Give the position of every malaria parasite and every leukocyte.
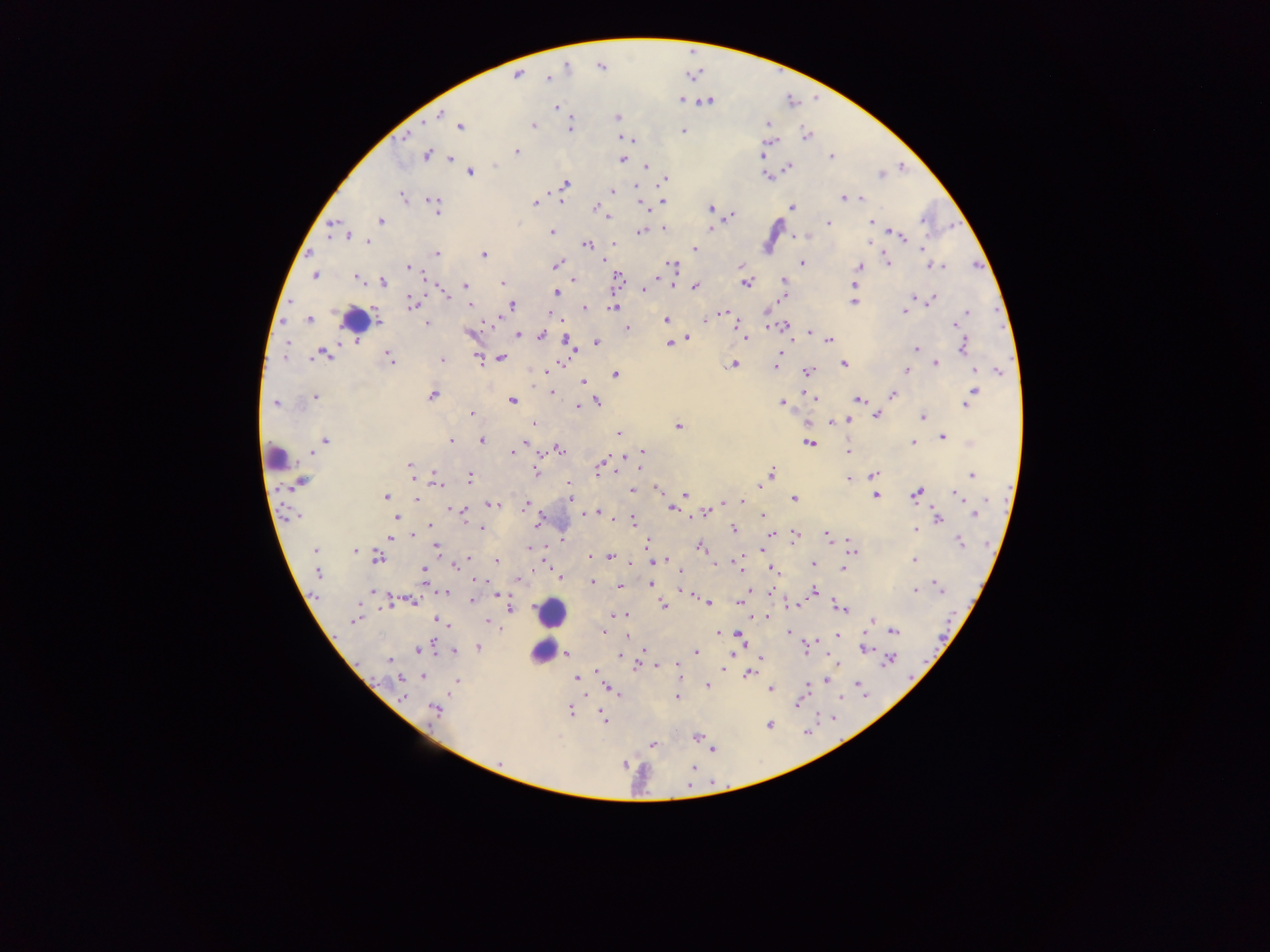
Approximate centers as x y in pixels.
Malaria parasites: 567 69; 517 75; 547 78; 680 100; 708 101; 558 107; 617 116; 436 117; 534 124; 766 125; 459 126; 570 129; 685 131; 806 134; 404 139; 769 140; 516 151; 426 154; 765 155; 831 155; 623 158; 646 165; 789 168; 471 171; 880 174; 770 176; 665 179; 566 182; 635 188; 612 192; 400 196; 862 198; 844 199; 430 200; 534 201; 560 202; 663 202; 437 205; 595 207; 791 207; 645 208; 708 209; 732 215; 605 217; 379 219; 829 222; 870 222; 331 226; 711 227; 662 229; 550 231; 639 231; 898 235; 367 243; 868 243; 588 244; 693 247; 922 248; 437 253; 483 255; 308 256; 601 258; 889 262; 556 263; 802 263; 673 265; 860 266; 406 267; 938 267; 313 276; 354 277; 619 279; 384 281; 425 281; 501 281; 573 282; 747 283; 463 285; 673 285; 854 285; 694 287; 643 289; 558 292; 448 297; 914 297; 853 301; 930 302; 413 305; 471 307; 512 307; 613 308; 585 309; 966 311; 903 314; 715 315; 494 320; 665 320; 307 321; 427 323; 956 326; 627 329; 783 329; 809 331; 544 335; 517 336; 687 338; 745 338; 567 339; 829 339; 596 343; 669 346; 915 349; 963 349; 573 357; 391 358; 478 358; 441 359; 501 359; 935 361; 734 363; 844 363; 560 364; 775 369; 973 369; 906 370; 999 370; 807 372; 616 374; 584 381; 974 390; 551 393; 893 394; 433 397; 315 398; 813 398; 859 400; 513 402; 782 402; 275 403; 598 403; 577 407; 964 407; 471 414; 877 415; 924 417; 848 420; 534 423; 678 425; 617 434; 942 437; 324 439; 481 439; 450 440; 914 441; 809 442; 522 445; 642 449; 561 450; 847 451; 512 453; 312 456; 601 463; 409 464; 598 468; 639 469; 536 470; 772 470; 972 474; 433 475; 872 476; 472 477; 849 479; 414 480; 302 481; 569 485; 288 486; 440 487; 757 487; 631 489; 656 490; 874 494; 915 494; 959 494; 686 495; 386 497; 571 497; 414 498; 793 498; 989 499; 490 503; 526 503; 738 503; 721 506; 457 510; 671 510; 596 511; 708 511; 463 512; 582 514; 974 514; 763 517; 939 517; 292 518; 395 518; 615 519; 631 519; 433 525; 535 526; 480 530; 915 530; 734 531; 392 535; 770 535; 795 537; 827 537; 849 539; 960 542; 436 548; 700 548; 313 550; 354 551; 853 551; 759 553; 609 556; 589 557; 377 558; 469 558; 737 558; 914 561; 495 562; 547 562; 654 563; 811 565; 455 566; 844 568; 424 569; 773 569; 318 575; 558 577; 473 579; 425 583; 652 584; 935 584; 585 585; 373 590; 815 590; 496 591; 771 592; 914 592; 445 594; 315 595; 690 595; 470 599; 415 602; 708 603; 739 603; 662 605; 795 606; 387 608; 511 609; 842 610; 613 614; 619 614; 766 617; 437 620; 354 622; 485 623; 869 623; 446 624; 893 631; 603 632; 723 633; 789 633; 736 635; 837 637; 433 643; 743 644; 864 647; 479 648; 643 649; 806 651; 454 652; 696 653; 735 653; 566 655; 620 656; 892 660; 388 662; 837 662; 657 664; 672 666; 723 670; 749 675; 401 678; 457 678; 423 679; 827 681; 856 681; 578 682; 805 685; 707 686; 608 689; 771 690; 864 694; 404 695; 677 697; 798 705; 435 709; 571 711; 832 719; 769 724; 653 744; 499 760.
Leukocytes: 353 324; 277 454; 556 613; 543 649.

Collected in Ghana. Image is 1270×952 pixels. Thick blood smear. One field of view. Photographed through a microscope with a mobile-phone camera.